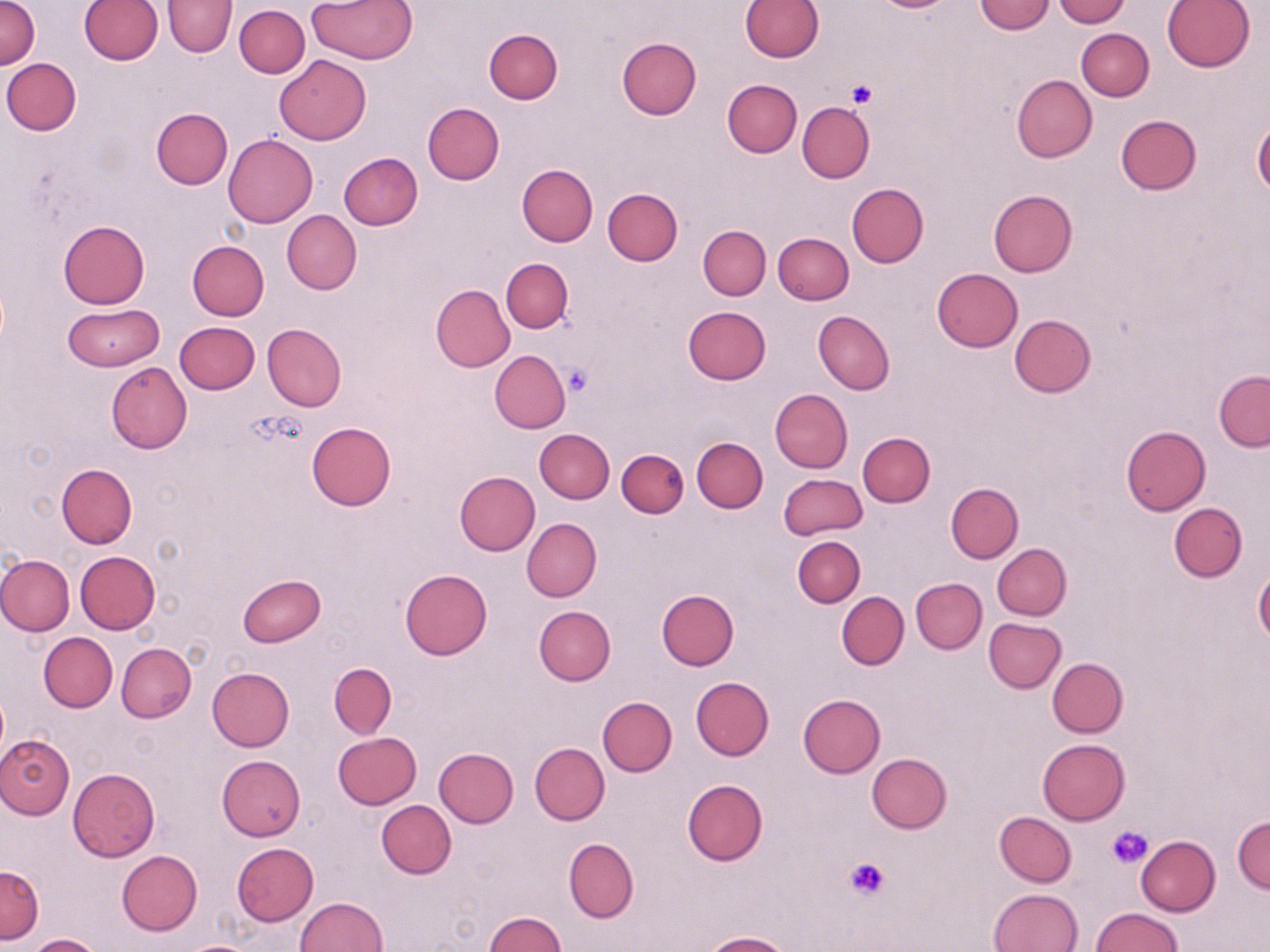
Approximate bounding boxes as [x1, y1, x2, y2] in pixels. Uninfected red blood cell locations: [739, 0, 822, 62], [975, 0, 1055, 34], [1053, 0, 1129, 26], [1, 1, 41, 69], [79, 1, 162, 65], [163, 1, 237, 57], [307, 1, 418, 64], [1163, 1, 1254, 72], [234, 5, 309, 78], [484, 28, 563, 103], [1076, 28, 1154, 101], [616, 36, 701, 121], [274, 55, 371, 145], [2, 58, 81, 134], [1011, 75, 1097, 161], [721, 79, 801, 158], [798, 101, 875, 182], [422, 102, 504, 185], [151, 108, 232, 189], [1115, 115, 1202, 195], [1253, 122, 1270, 196], [223, 133, 318, 227], [339, 153, 423, 229], [517, 163, 598, 247], [846, 183, 927, 268], [603, 187, 682, 266], [987, 190, 1078, 277], [282, 210, 361, 294], [58, 219, 149, 308], [698, 225, 770, 300], [772, 232, 853, 305], [186, 240, 269, 320], [501, 259, 573, 333], [931, 268, 1023, 352], [430, 285, 514, 372], [62, 304, 163, 372], [683, 307, 771, 384], [813, 310, 894, 395], [1009, 314, 1095, 397], [174, 322, 260, 394], [263, 323, 346, 413], [489, 350, 570, 433], [106, 362, 192, 453], [1213, 371, 1270, 450], [770, 388, 853, 473], [307, 422, 396, 510], [1121, 426, 1209, 515], [535, 428, 615, 503], [857, 432, 935, 507], [692, 437, 767, 512], [616, 448, 688, 518], [57, 463, 138, 548], [454, 470, 539, 555], [778, 473, 867, 540], [946, 482, 1023, 563], [1168, 502, 1246, 582], [522, 517, 601, 602], [793, 536, 865, 607], [991, 543, 1071, 620], [75, 551, 160, 634], [0, 554, 74, 636], [1254, 567, 1270, 646], [400, 569, 492, 659], [237, 574, 326, 647], [910, 577, 987, 654], [838, 587, 985, 659], [656, 589, 738, 670], [837, 592, 908, 669], [534, 606, 615, 685], [983, 618, 1066, 692], [39, 632, 116, 712], [116, 643, 196, 723], [1047, 657, 1127, 737], [329, 663, 397, 738], [206, 667, 294, 751], [691, 677, 774, 760], [798, 693, 885, 777], [597, 696, 677, 776], [332, 732, 422, 809], [0, 733, 75, 820], [1037, 739, 1129, 825], [529, 742, 609, 825], [434, 748, 518, 827], [866, 752, 951, 832], [217, 755, 305, 839], [68, 767, 160, 861], [682, 779, 767, 865], [377, 800, 456, 878], [995, 811, 1076, 886], [1232, 815, 1270, 893], [1135, 836, 1219, 916], [563, 839, 638, 923], [232, 843, 318, 925], [116, 849, 203, 935], [0, 864, 44, 945], [990, 888, 1083, 952], [295, 897, 388, 951], [1093, 909, 1185, 952], [485, 913, 568, 951], [704, 931, 793, 952], [26, 934, 104, 952], [177, 940, 264, 952]. Platelet locations: [846, 79, 876, 109], [563, 365, 592, 396], [1107, 825, 1152, 867], [844, 856, 891, 901]. Slide-level diagnosis: no evidence of blood parasites. Image is 1270×952 pixels. May-Grünwald-Giemsa stain. One field of a larger specimen. Thin blood film. Optical microscopy. Captured at 1000x magnification.